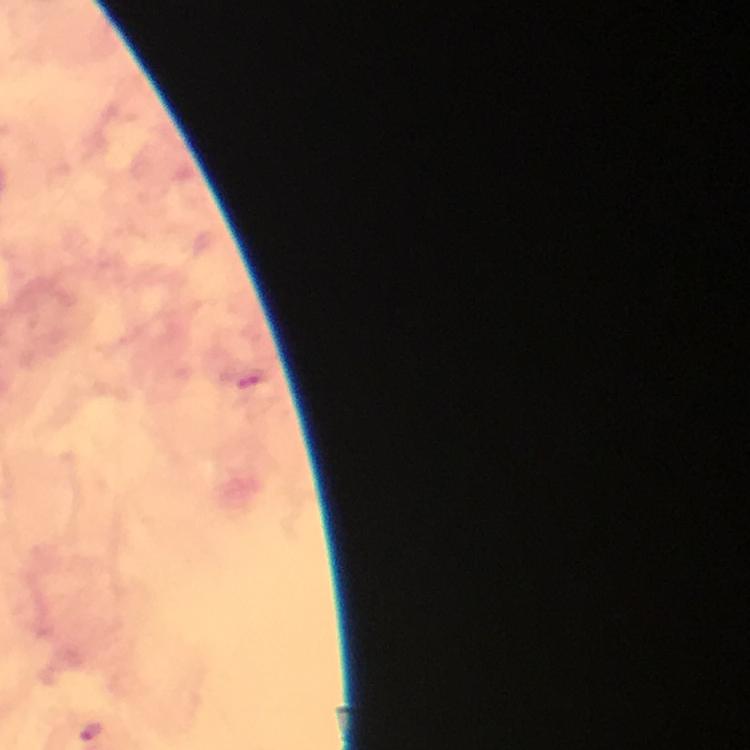

{
  "stain": "Giemsa",
  "preparation": "thick smear",
  "image_size": "750×750 pixels",
  "cropped_from": "a single field of view",
  "capture": "smartphone mounted on the microscope",
  "context": "from a diagnostic examination for malaria",
  "magnification": "100x",
  "plasmodium_parasite_locations": "approximate centers as [x, y] in pixels: [92, 732]",
  "immersion_oil": "used"
}